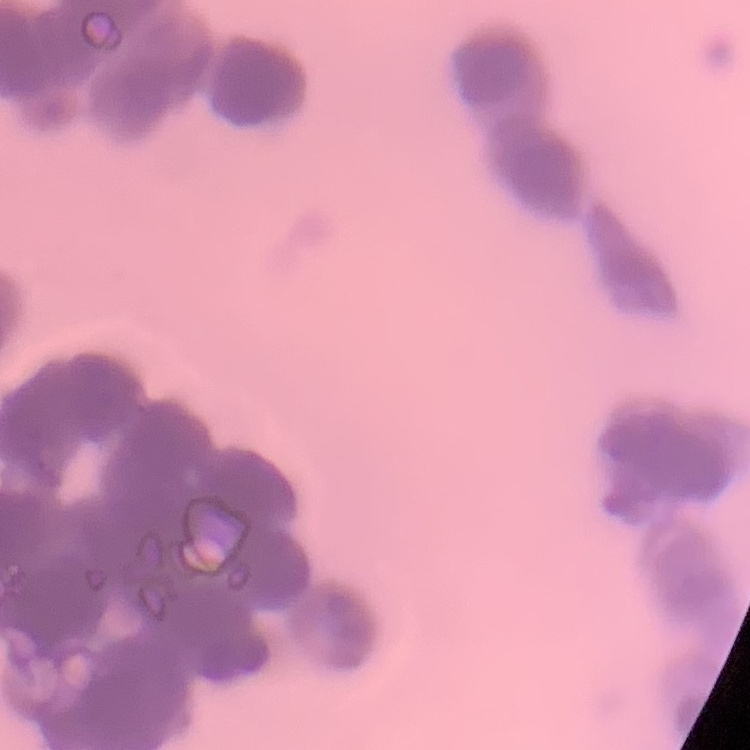

The red blood cells exhibit rouleaux formation. Stained with either Field's or Giemsa. One tile cut from a larger photomicrograph. Thin blood smear.